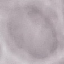

Summary:
  - Result: no malaria parasites seen
  - Stain: Giemsa
  - Image type: cell patch, automatically extracted from a larger field of view and resized to 64 × 64 pixels
  - Preparation: thin blood smear
  - Capture: smartphone camera at the microscope eyepiece